State the blood parasite species.
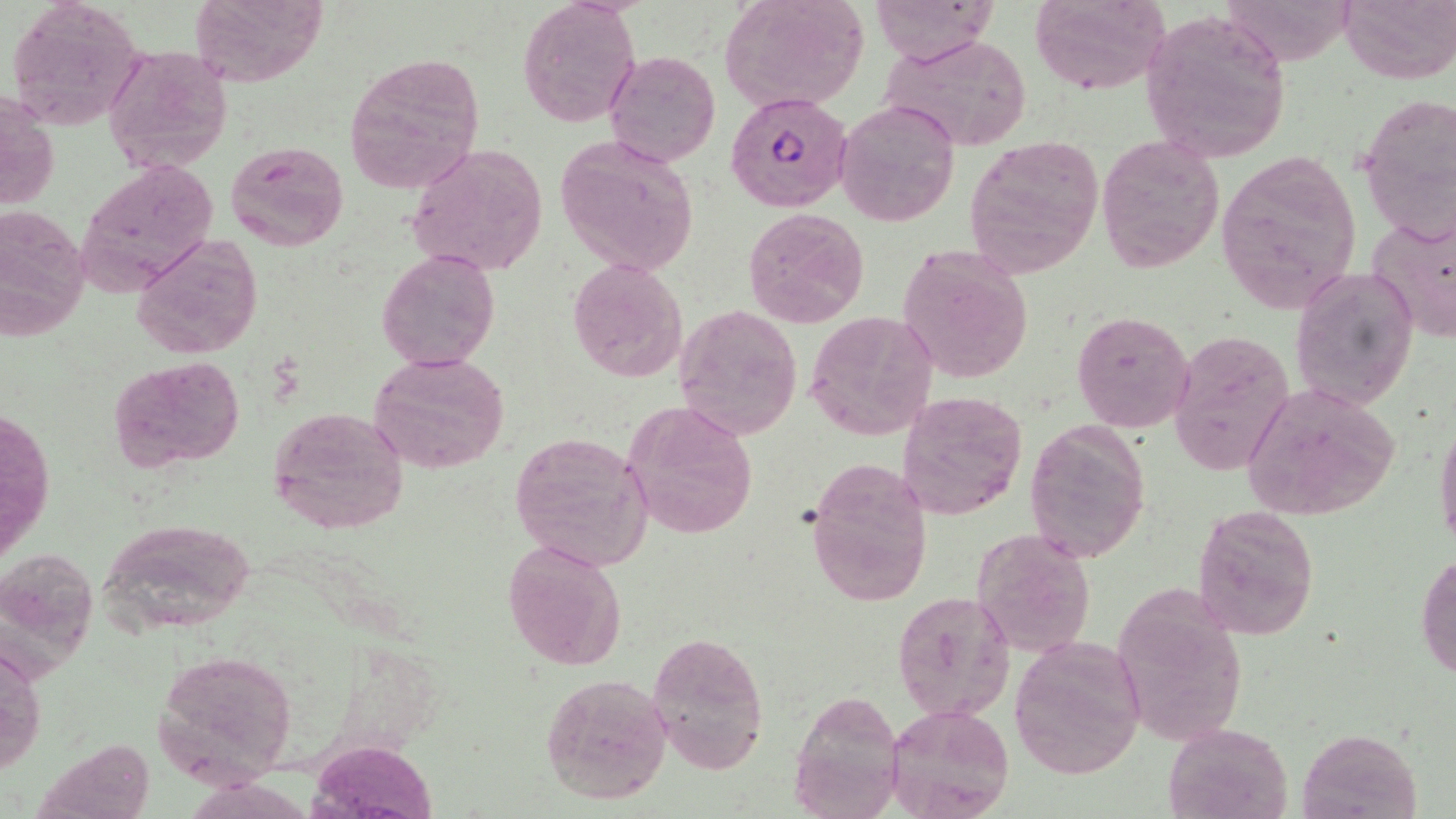
Plasmodium falciparum.

magnification = 1000x
preparation = thin blood film
image size = 1456×819 pixels
Plasmodium falciparum-infected red blood cell locations = approximate bounding boxes as named x1/y1/x2/y2 corners in pixels: (x1=725, y1=90, x2=853, y2=211)
uninfected red blood cell locations = approximate bounding boxes as named x1/y1/x2/y2 corners in pixels: (x1=6, y1=0, x2=149, y2=134), (x1=188, y1=0, x2=328, y2=88), (x1=719, y1=0, x2=869, y2=114), (x1=869, y1=0, x2=999, y2=66), (x1=1029, y1=0, x2=1172, y2=96), (x1=1220, y1=0, x2=1355, y2=65), (x1=1339, y1=0, x2=1456, y2=84), (x1=516, y1=2, x2=640, y2=128), (x1=1140, y1=11, x2=1291, y2=163), (x1=879, y1=32, x2=1034, y2=153), (x1=104, y1=45, x2=234, y2=173), (x1=605, y1=50, x2=721, y2=166), (x1=342, y1=52, x2=486, y2=198), (x1=1, y1=89, x2=58, y2=212), (x1=1357, y1=91, x2=1454, y2=242), (x1=836, y1=101, x2=960, y2=227), (x1=556, y1=134, x2=700, y2=275), (x1=1095, y1=136, x2=1224, y2=272), (x1=963, y1=138, x2=1105, y2=280), (x1=225, y1=140, x2=347, y2=251), (x1=407, y1=142, x2=550, y2=279), (x1=1216, y1=151, x2=1362, y2=313), (x1=77, y1=156, x2=221, y2=291), (x1=0, y1=207, x2=92, y2=340), (x1=742, y1=207, x2=871, y2=330), (x1=1365, y1=213, x2=1455, y2=345), (x1=132, y1=232, x2=262, y2=360), (x1=897, y1=244, x2=1033, y2=384), (x1=377, y1=249, x2=500, y2=372), (x1=567, y1=257, x2=689, y2=384), (x1=1289, y1=265, x2=1419, y2=411), (x1=672, y1=303, x2=803, y2=441), (x1=1071, y1=310, x2=1194, y2=432), (x1=803, y1=311, x2=937, y2=441), (x1=1167, y1=329, x2=1294, y2=475), (x1=371, y1=351, x2=510, y2=473), (x1=108, y1=355, x2=246, y2=474), (x1=1238, y1=382, x2=1403, y2=522), (x1=898, y1=389, x2=1028, y2=523), (x1=623, y1=400, x2=759, y2=542), (x1=268, y1=405, x2=410, y2=535), (x1=1434, y1=410, x2=1456, y2=556), (x1=1025, y1=418, x2=1149, y2=564), (x1=509, y1=431, x2=653, y2=571), (x1=804, y1=457, x2=933, y2=607), (x1=1193, y1=505, x2=1320, y2=639), (x1=96, y1=517, x2=258, y2=635), (x1=972, y1=528, x2=1096, y2=660), (x1=502, y1=540, x2=626, y2=671), (x1=1417, y1=550, x2=1456, y2=682), (x1=1112, y1=580, x2=1246, y2=746), (x1=892, y1=590, x2=1015, y2=721), (x1=646, y1=630, x2=770, y2=775), (x1=1009, y1=636, x2=1147, y2=782), (x1=0, y1=637, x2=45, y2=780), (x1=154, y1=647, x2=298, y2=784), (x1=540, y1=672, x2=673, y2=805), (x1=792, y1=690, x2=907, y2=817), (x1=885, y1=703, x2=1016, y2=819), (x1=1163, y1=722, x2=1293, y2=818), (x1=1297, y1=727, x2=1421, y2=818), (x1=312, y1=740, x2=437, y2=816)
modality = optical microscopy
stain = May-Grünwald-Giemsa
field of view = one of a larger specimen